Name the parasite shown.
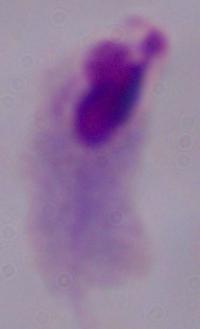

A trichomonad.

Photomicrograph. Captured at 1000x magnification.